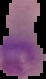 Image is 46×79 pixels. Segmented cell region on a black background. From a thin blood film. Result: malaria parasites identified.